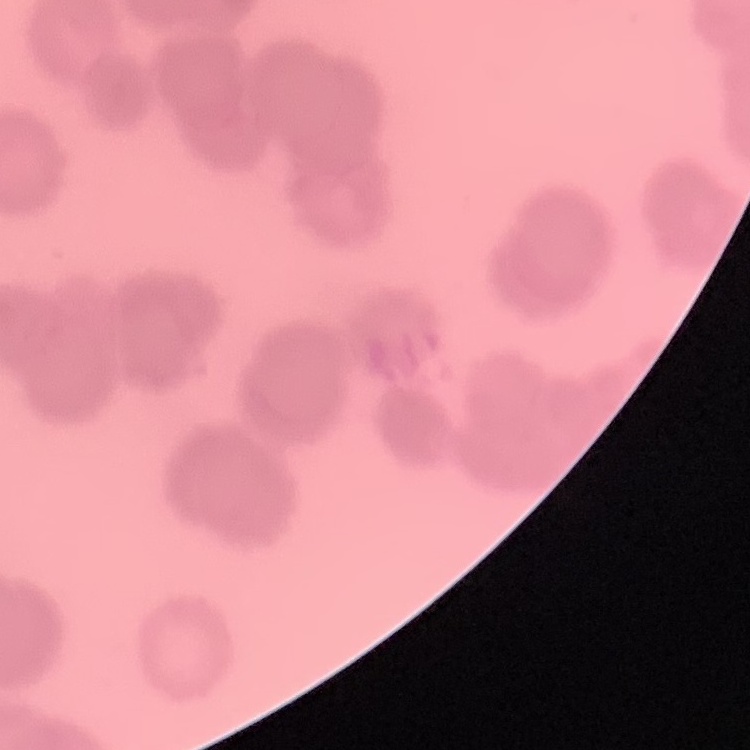

Summary:
  - Red blood cell morphology: rouleaux formation
  - Stain: Field's or Giemsa
  - Preparation: thin blood film
  - Image type: one tile cut from a larger photomicrograph